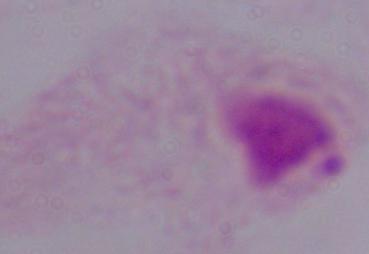

1000x magnification. Photomicrograph. A trichomonad is seen.